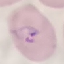
result = malaria parasites identified
image type = automatically extracted cell patch, resized to 64 × 64 pixels
stain = Giemsa
preparation = thin blood smear
capture = smartphone through the microscope eyepiece